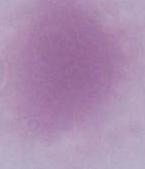
Summary:
  - Modality: photomicrograph
  - Identification: red blood cell
  - Magnification: 1000x